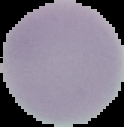
preparation = thin blood film
image type = segmented cell region with the area outside set to black
malaria status = uninfected
image size = 124×127 pixels